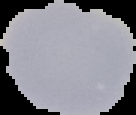 The area outside the segmented cell region is set to black. Image is 136×115 pixels. From a thin blood film. Result: no Plasmodium parasites detected.